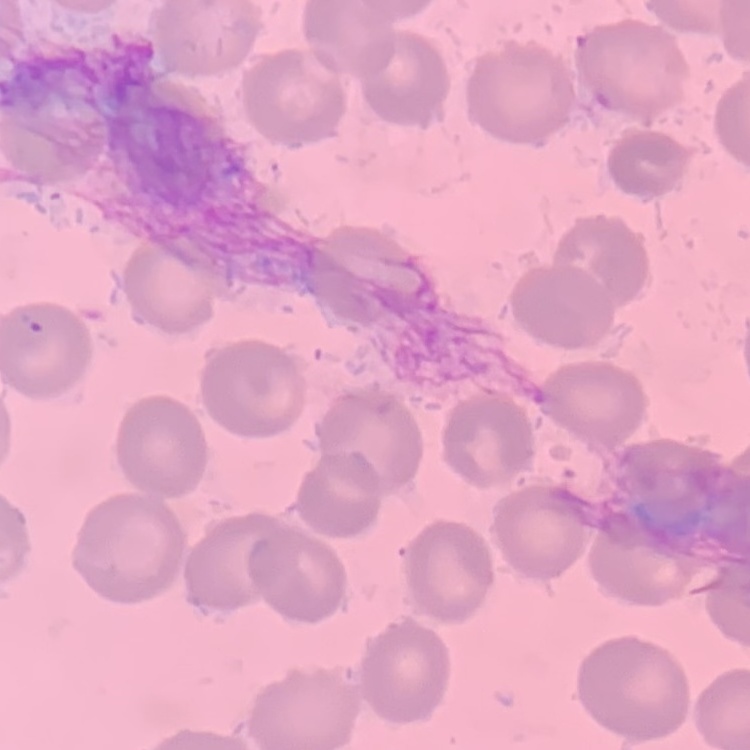
red blood cell morphology = no rouleaux formation
image type = one tile cut from a larger photomicrograph
stain = Field's or Giemsa
preparation = thin blood film